Point out each leukocyte.
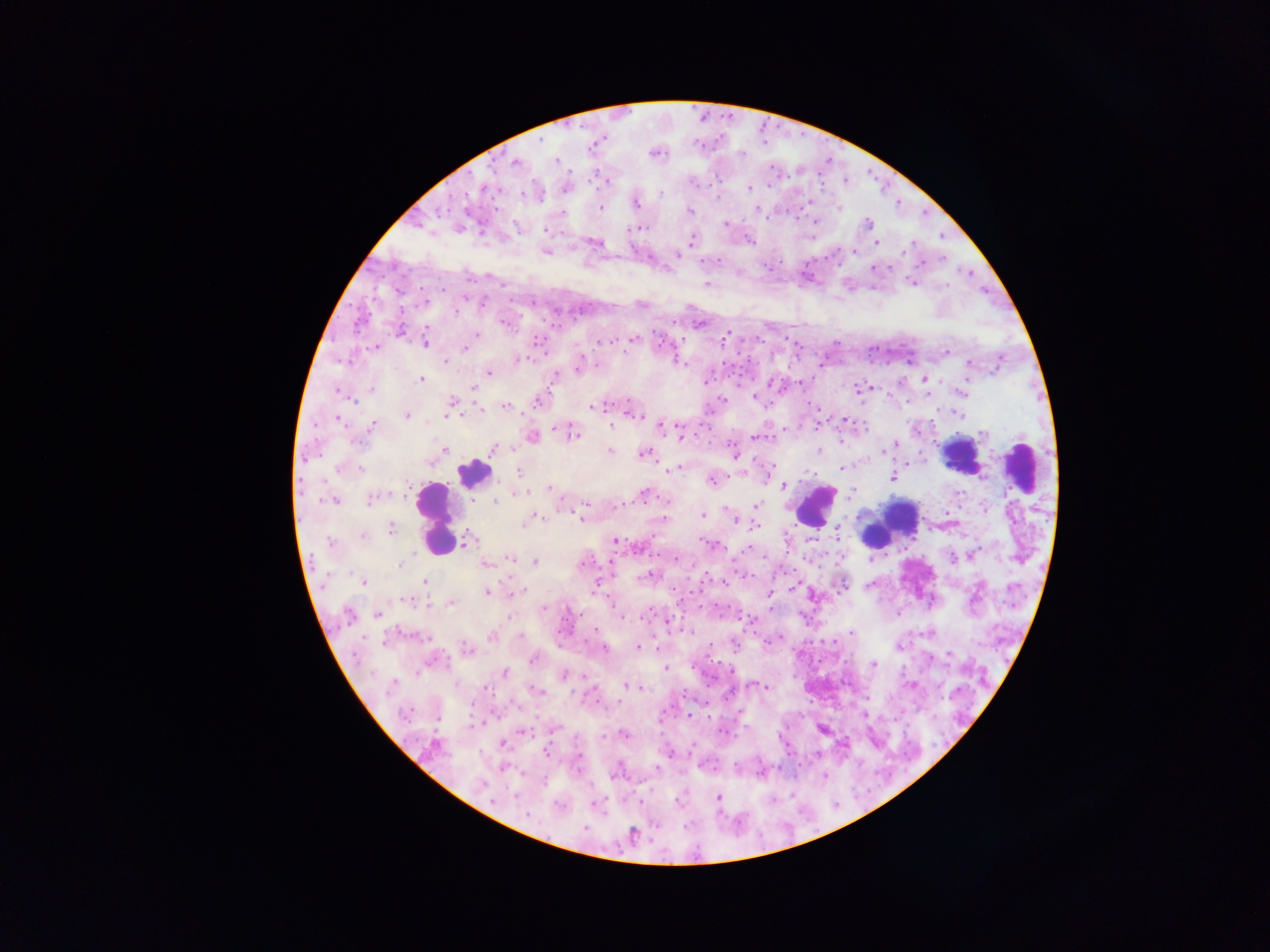
Approximate centers as {x, y} in pixels.
Leukocytes: {963, 455}, {1021, 467}, {471, 473}, {815, 506}, {901, 515}, {435, 518}, {890, 523}.

Plasmodium parasite locations (subset; some below the resolvable size): {595, 143}, {655, 153}, {556, 159}, {515, 162}, {604, 178}, {566, 187}, {749, 187}, {662, 193}, {536, 194}, {809, 202}, {635, 203}, {599, 208}, {839, 208}, {758, 209}, {689, 210}, {925, 212}, {816, 220}, {727, 224}, {868, 224}, {637, 227}, {517, 229}, {942, 236}, {692, 239}, {748, 240}, {594, 242}, {913, 242}, {877, 243}, {854, 249}, {545, 250}, {903, 252}, {677, 255}, {944, 258}, {719, 259}, {701, 261}, {780, 261}, {922, 263}, {764, 265}, {873, 268}, {959, 268}, {891, 269}, {770, 271}, {971, 273}, {911, 282}, {502, 284}, {708, 284}, {948, 285}, {420, 287}, {985, 288}, {405, 292}, {486, 296}, {513, 300}, {372, 302}, {428, 302}, {351, 303}, {533, 303}, {642, 304}, {401, 305}, {482, 305}, {419, 308}, {371, 312}, {337, 316}, {359, 319}, {544, 319}, {674, 320}, {506, 322}, {698, 323}, {554, 324}, {560, 326}, {398, 329}, {360, 331}, {654, 331}, {536, 335}, {786, 335}, {726, 336}, {473, 337}, {545, 337}, {333, 338}, {632, 339}, {742, 339}, {598, 340}, {614, 340}, {684, 340}, {762, 340}, {425, 342}, {658, 343}, {795, 343}, {837, 343}, {535, 344}, {466, 346}, {375, 347}, {905, 347}, {801, 348}, {878, 350}, {887, 351}, {546, 352}, {738, 353}, {947, 353}, {868, 356}, {998, 356}, {828, 357}, {340, 358}, {675, 358}, {748, 359}, {517, 360}, {888, 360}, {446, 361}, {723, 362}, {910, 362}, {969, 362}, {579, 364}, {598, 366}, {734, 366}, {818, 367}, {998, 368}, {790, 369}, {489, 373}, {554, 377}, {728, 377}, {420, 379}, {924, 379}, {704, 381}, {801, 381}, {795, 382}, {338, 386}, {739, 386}, {870, 386}, {472, 387}, {373, 390}, {860, 390}, {961, 391}, {928, 395}, {755, 397}, {357, 400}, {724, 400}, {808, 401}, {906, 401}, {538, 402}, {709, 404}, {506, 406}, {595, 406}, {451, 407}, {477, 407}, {819, 408}, {938, 410}, {631, 411}, {958, 413}, {705, 414}, {406, 415}, {449, 415}, {338, 418}, {844, 419}, {931, 421}, {817, 422}, {316, 424}, {700, 425}, {661, 426}, {371, 427}, {784, 427}, {815, 429}, {920, 432}, {571, 433}, {679, 434}, {694, 434}, {774, 435}, {532, 436}, {756, 437}, {317, 439}, {710, 440}, {361, 441}, {892, 445}, {730, 446}, {887, 448}, {443, 449}, {493, 449}, {819, 450}, {609, 451}, {320, 454}, {644, 454}, {733, 455}, {907, 463}, {338, 467}, {840, 468}, {670, 469}, {519, 471}, {730, 477}, {892, 477}, {712, 479}, {783, 485}, {550, 488}, {391, 490}, {517, 493}, {850, 493}, {645, 494}, {374, 497}, {334, 500}, {494, 502}, {586, 503}, {623, 505}, {756, 506}, {960, 507}, {571, 511}, {947, 513}, {703, 515}, {582, 516}, {535, 517}, {664, 519}, {735, 520}, {752, 521}, {759, 527}, {390, 530}, {751, 530}, {836, 530}, {362, 535}, {652, 536}, {700, 539}, {615, 541}, {464, 542}, {713, 544}, {636, 546}, {979, 547}, {750, 548}, {783, 551}, {743, 553}, {658, 555}, {765, 557}, {508, 558}, {592, 558}, {733, 558}, {805, 558}, {953, 558}, {676, 560}, {535, 561}, {581, 561}, {610, 562}, {485, 564}, {400, 565}, {599, 568}, {794, 570}, {735, 571}, {708, 572}, {786, 573}, {613, 575}, {775, 575}, {650, 576}, {753, 576}, {741, 578}, {723, 579}, {870, 580}, {364, 581}, {425, 582}, {701, 582}, {712, 582}, {597, 583}, {843, 584}, {727, 585}, {702, 590}, {487, 591}, {674, 591}, {691, 592}, {513, 593}, {769, 593}, {791, 593}, {812, 596}, {606, 597}, {407, 600}, {681, 600}, {1007, 601}, {450, 603}, {701, 604}, {716, 604}, {427, 605}, {728, 606}, {1014, 607}, {543, 608}, {614, 609}, {773, 609}, {648, 610}, {684, 610}, {741, 611}, {348, 614}, {376, 614}, {898, 615}, {580, 616}, {720, 616}, {640, 617}, {681, 617}, {563, 618}, {621, 618}, {741, 618}, {758, 619}, {805, 619}, {667, 620}, {648, 621}, {574, 627}, {597, 629}, {681, 631}, {851, 631}, {399, 632}, {558, 632}, {693, 632}, {756, 632}, {364, 634}, {492, 636}, {779, 637}, {429, 639}, {834, 639}, {585, 640}, {733, 640}, {822, 640}, {383, 641}, {422, 641}, {711, 643}, {810, 644}, {605, 647}, {636, 647}, {443, 648}, {657, 648}, {465, 649}, {999, 650}, {735, 651}, {950, 655}, {706, 656}, {448, 658}, {533, 658}, {818, 658}, {435, 659}, {719, 663}, {1007, 663}, {873, 664}, {692, 666}, {665, 669}, {730, 672}, {418, 673}, {504, 673}, {564, 675}, {703, 676}, {584, 677}, {713, 678}, {393, 684}, {458, 685}, {626, 685}, {912, 685}, {594, 686}, {756, 686}, {761, 686}, {637, 687}, {487, 688}, {708, 688}, {538, 690}, {493, 695}, {684, 695}, {726, 698}, {512, 701}, {472, 702}, {598, 702}, {620, 702}, {708, 703}, {671, 706}, {517, 707}, {607, 709}, {413, 710}, {492, 711}, {741, 711}, {468, 715}, {690, 715}, {709, 716}, {499, 717}, {439, 721}, {661, 721}, {483, 723}, {475, 725}, {553, 728}, {822, 728}, {726, 730}, {523, 733}, {739, 733}, {623, 734}, {434, 744}, {503, 745}, {693, 745}, {843, 745}, {546, 752}, {669, 754}, {817, 755}, {503, 767}, {655, 767}, {780, 769}, {761, 772}, {889, 773}, {825, 774}, {869, 791}, {793, 792}, {651, 793}, {717, 797}, {675, 800}, {837, 802}, {640, 803}, {594, 804}, {800, 806}, {583, 828}, {632, 835}. Image is 1270×952 pixels. Mobile-phone photograph taken through the microscope. Thick blood film. One field of view. Collected in Ghana.